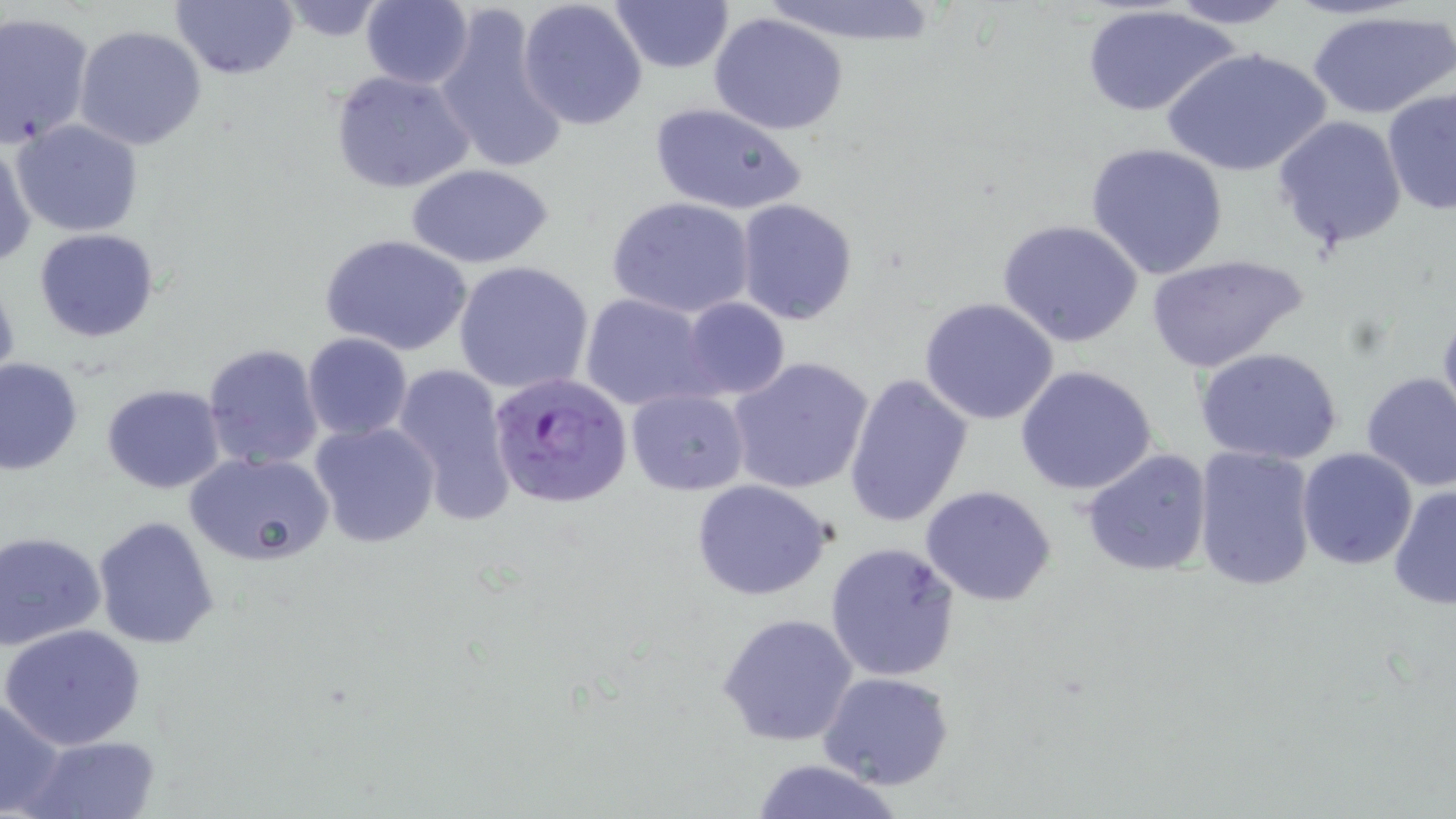
Approximate bounding boxes as (x1,y1)-(x2,y2) corner pairs in pixels. Uninfected red blood cell locations: (759,0)-(942,45), (1158,0)-(1301,28), (169,1)-(299,81), (273,1)-(395,41), (359,1)-(475,89), (516,1)-(649,130), (607,1)-(735,75), (434,6)-(570,177), (1079,6)-(1240,119), (1306,8)-(1456,120), (0,11)-(94,150), (709,12)-(849,135), (74,25)-(206,150), (1161,46)-(1334,178), (329,69)-(475,194), (1380,88)-(1456,217), (649,101)-(808,217), (1272,115)-(1408,256), (12,119)-(145,236), (1,137)-(36,271), (1085,144)-(1229,282), (408,163)-(554,269), (606,195)-(755,319), (734,197)-(859,326), (996,218)-(1143,347), (33,227)-(159,343), (319,233)-(475,357), (1145,252)-(1307,372), (453,260)-(595,396), (0,270)-(21,397), (579,292)-(715,413), (681,297)-(789,400), (918,297)-(1061,426), (1436,306)-(1456,431), (302,333)-(412,441), (203,342)-(325,470), (1194,346)-(1346,464), (727,355)-(875,495), (0,357)-(84,476), (392,362)-(517,526), (1015,366)-(1159,497), (842,371)-(975,529), (1357,373)-(1456,492), (102,385)-(225,494), (625,388)-(749,495), (307,419)-(443,550), (1193,446)-(1318,591), (1296,446)-(1419,570), (1081,449)-(1215,577), (189,453)-(333,567), (692,480)-(835,602), (1388,482)-(1456,612), (919,485)-(1060,606), (92,515)-(220,648), (1,533)-(105,648), (824,542)-(961,682), (717,613)-(858,746), (3,623)-(147,750), (819,673)-(955,791), (1,694)-(66,817), (23,733)-(159,817), (747,758)-(907,818). Plasmodium falciparum-infected red blood cell locations: (488,371)-(634,508). Slide-level diagnosis: Plasmodium falciparum. Thin blood film. Image is 1456×819 pixels. Optical microscopy. May-Grünwald-Giemsa stain. Single field of view. Captured at 1000x magnification.